Locate and identify every blood parasite.
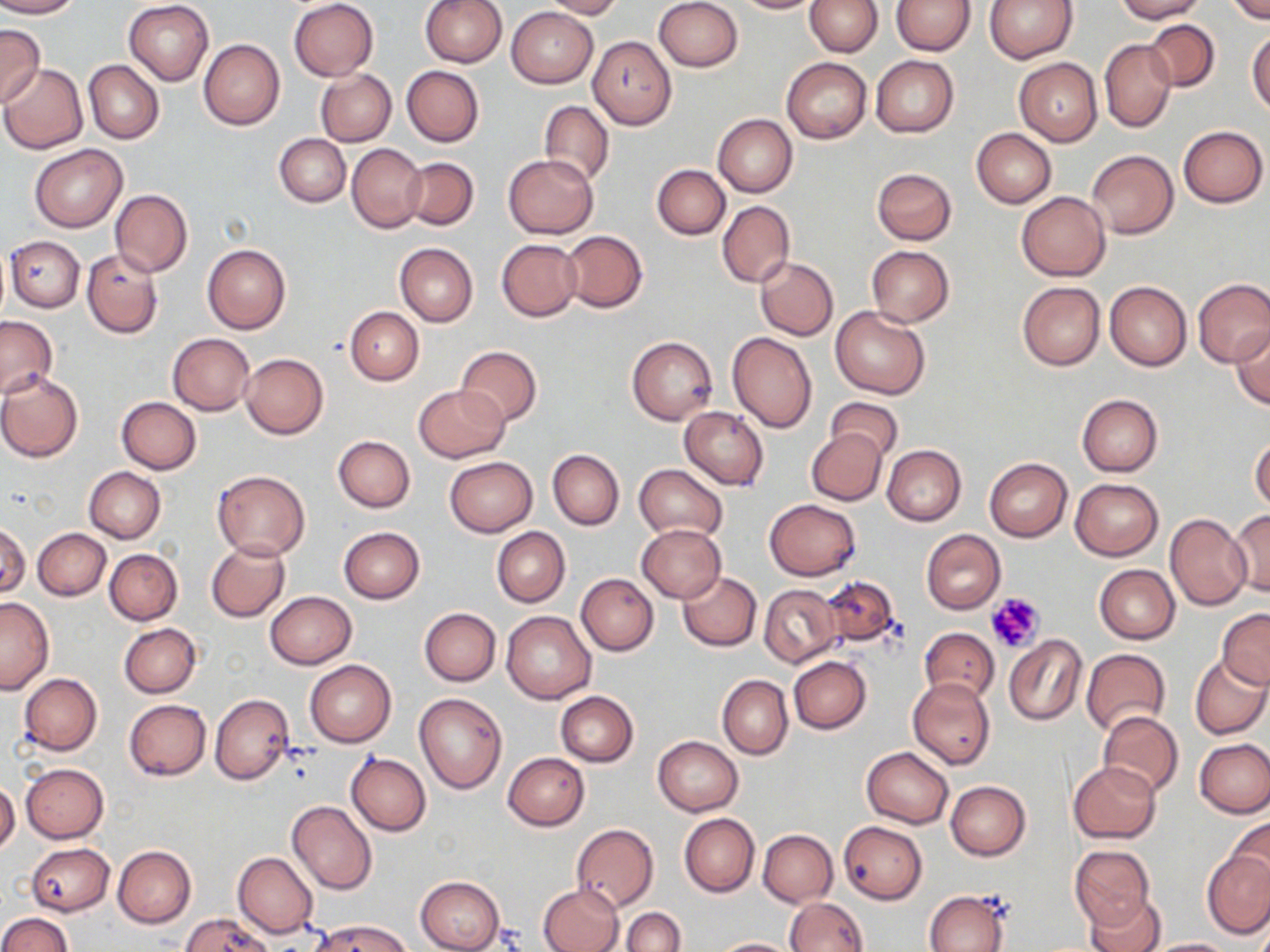
No blood parasites seen.

Summary:
  - Coordinate format: approximate bounding boxes as [x1, y1, x2, y2] in pixels
  - Uninfected red blood cell locations: [0, 0, 80, 18], [419, 0, 506, 68], [540, 0, 624, 18], [731, 0, 819, 14], [806, 0, 883, 56], [893, 0, 975, 54], [985, 0, 1078, 63], [1116, 0, 1207, 21], [1226, 0, 1270, 24], [123, 1, 213, 85], [288, 1, 379, 81], [655, 1, 742, 72], [506, 6, 597, 88], [1145, 19, 1219, 91], [0, 23, 45, 112], [1247, 29, 1270, 115], [587, 36, 676, 128], [199, 38, 285, 130], [1099, 38, 1176, 133], [870, 56, 959, 136], [782, 57, 871, 143], [1014, 58, 1102, 145], [83, 59, 163, 144], [0, 64, 88, 154], [402, 66, 484, 146], [315, 68, 396, 146], [538, 101, 614, 187], [712, 114, 797, 197], [1178, 125, 1268, 207], [971, 129, 1056, 208], [275, 134, 350, 207], [347, 144, 426, 231], [29, 145, 127, 232], [1087, 150, 1178, 238], [502, 153, 599, 238], [403, 157, 478, 230], [652, 164, 729, 240], [872, 167, 957, 246], [109, 189, 193, 277], [1017, 191, 1110, 280], [718, 201, 795, 288], [561, 230, 647, 312], [5, 236, 84, 313], [496, 239, 582, 322], [203, 243, 291, 335], [394, 243, 477, 327], [866, 246, 953, 326], [81, 249, 163, 337], [755, 257, 838, 340], [1193, 278, 1270, 368], [1104, 280, 1191, 371], [1017, 282, 1104, 371], [346, 306, 423, 385], [831, 306, 930, 400], [1, 315, 55, 398], [1230, 326, 1270, 409], [727, 332, 817, 435], [167, 333, 255, 416], [626, 336, 718, 424], [455, 345, 543, 426], [240, 353, 328, 438], [0, 372, 83, 462], [414, 384, 509, 462], [1076, 394, 1163, 476], [117, 397, 201, 474], [825, 398, 902, 464], [679, 407, 769, 490], [805, 428, 887, 505], [332, 435, 415, 512], [1250, 435, 1270, 513], [882, 445, 966, 525], [547, 449, 624, 530], [444, 457, 537, 537], [984, 458, 1072, 542], [633, 464, 727, 543], [84, 467, 165, 542], [211, 468, 311, 561], [1070, 478, 1163, 560], [764, 499, 861, 580], [1230, 510, 1270, 596], [1165, 513, 1253, 610], [0, 522, 30, 599], [637, 524, 725, 602], [338, 527, 425, 603], [492, 527, 570, 606], [33, 528, 110, 600], [921, 529, 1005, 615], [207, 540, 290, 622], [105, 548, 182, 625], [1094, 565, 1180, 644], [678, 571, 761, 651], [576, 573, 659, 656], [821, 575, 902, 648], [759, 584, 841, 667], [265, 591, 357, 669], [0, 597, 53, 692], [419, 607, 501, 686], [1218, 609, 1270, 688], [501, 610, 596, 703], [120, 623, 201, 698], [919, 628, 999, 703], [1004, 634, 1086, 726], [1081, 648, 1171, 738], [1190, 654, 1270, 740], [788, 656, 871, 733], [305, 660, 396, 747], [19, 673, 102, 754], [718, 675, 792, 759], [909, 678, 995, 770], [556, 691, 638, 766], [414, 692, 507, 794], [210, 693, 294, 785], [123, 699, 211, 780], [1098, 710, 1184, 797], [654, 735, 742, 816], [1195, 739, 1270, 818], [862, 747, 954, 828], [502, 752, 589, 830], [345, 753, 431, 836], [1068, 762, 1160, 843], [21, 764, 109, 843], [0, 781, 20, 855], [946, 781, 1031, 860], [287, 800, 376, 895], [679, 813, 759, 896], [1225, 816, 1270, 898], [839, 821, 927, 903], [571, 824, 659, 910], [758, 829, 837, 907], [25, 842, 114, 916], [113, 845, 196, 928], [1070, 846, 1154, 930], [1203, 849, 1270, 938], [232, 851, 317, 938], [416, 876, 504, 952], [538, 883, 624, 952], [925, 889, 1009, 952], [1085, 893, 1166, 952], [785, 897, 866, 951], [622, 907, 686, 952], [0, 913, 72, 952], [180, 915, 271, 952], [316, 919, 410, 952], [710, 937, 800, 951], [1145, 937, 1237, 951]
  - Platelet locations: [986, 592, 1044, 654]
  - Slide-level diagnosis: no evidence of blood parasites
  - Magnification: 1000x
  - Preparation: thin blood smear
  - Stain: May-Grünwald-Giemsa
  - Field of view: one of a larger specimen
  - Image size: 1270×952 pixels
  - Modality: optical microscopy